Locate every white blood cell.
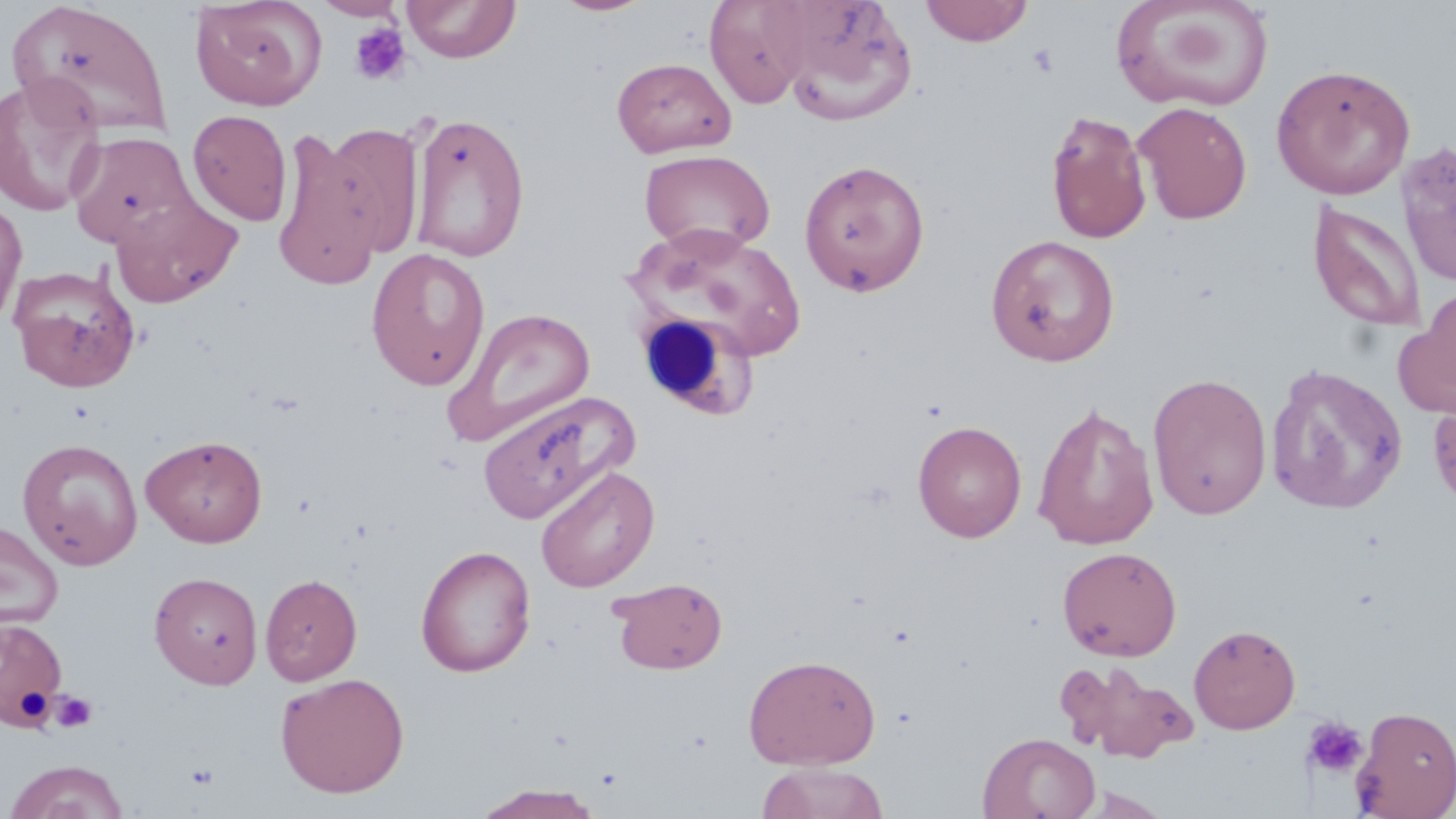

Approximate bounding boxes as [x1, y1, x2, y2] in pixels.
White blood cells: [636, 311, 755, 419].

Uninfected red blood cell locations: [190, 0, 325, 111], [313, 0, 407, 20], [402, 0, 521, 63], [550, 0, 656, 17], [704, 0, 812, 109], [920, 0, 1034, 46], [6, 1, 172, 138], [774, 1, 917, 125], [1110, 1, 1275, 113], [611, 56, 736, 158], [1271, 63, 1415, 200], [0, 75, 106, 217], [1133, 101, 1252, 224], [188, 109, 292, 226], [1046, 111, 1152, 244], [409, 112, 530, 262], [321, 121, 426, 259], [271, 126, 385, 291], [67, 130, 198, 249], [1396, 140, 1456, 287], [639, 149, 775, 256], [799, 158, 930, 296], [111, 195, 243, 308], [0, 197, 26, 330], [1308, 201, 1426, 331], [630, 225, 808, 367], [985, 233, 1120, 366], [366, 248, 491, 391], [9, 263, 141, 392], [1394, 289, 1456, 419], [443, 307, 596, 447], [1265, 362, 1408, 515], [1147, 372, 1272, 521], [477, 390, 637, 525], [1428, 390, 1456, 512], [1032, 402, 1160, 551], [913, 420, 1027, 542], [140, 434, 268, 547], [17, 438, 143, 570], [535, 464, 659, 593], [0, 520, 63, 630], [415, 545, 536, 677], [1057, 546, 1182, 661], [148, 572, 263, 689], [260, 574, 362, 686], [609, 576, 728, 674], [0, 616, 68, 729], [1189, 624, 1301, 734], [743, 653, 881, 769], [1058, 660, 1199, 763], [275, 672, 410, 798], [1351, 704, 1456, 819], [978, 732, 1101, 819], [5, 759, 130, 819], [754, 762, 891, 819], [471, 784, 607, 818], [1074, 788, 1175, 818]. Platelet locations: [349, 23, 411, 85], [48, 690, 98, 733], [1302, 716, 1368, 778]. Slide-level diagnosis: no evidence of blood parasites. Image is 1456×819 pixels. One field of a larger specimen. Thin blood smear. Light microscopy. 1000x magnification. May-Grünwald-Giemsa stain.